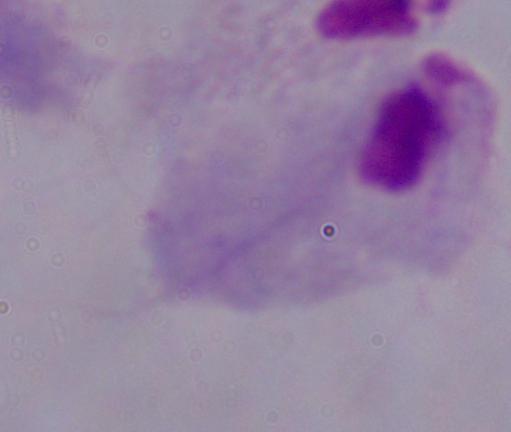 1000x magnification. Micrograph. A trichomonad is shown.